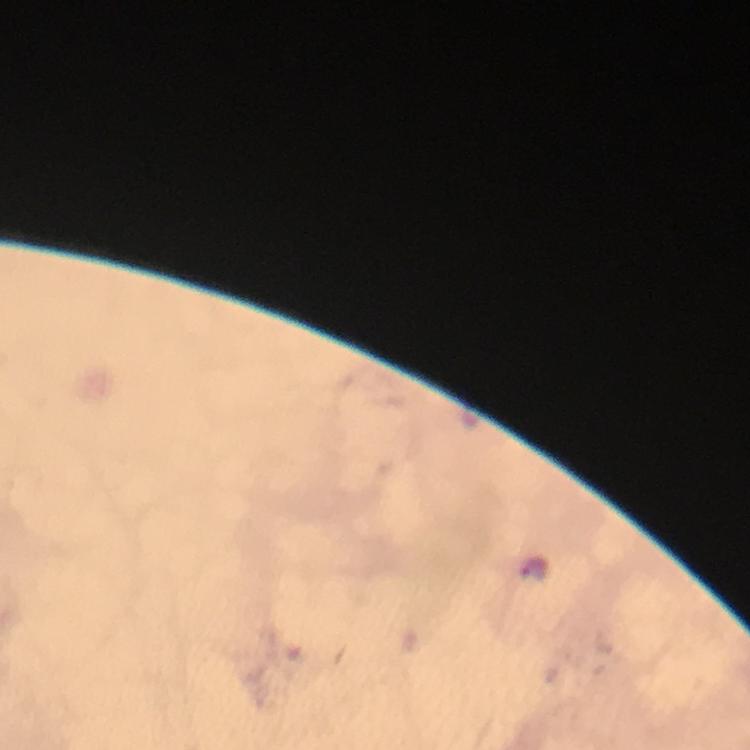
Approximate centers as (x, y) in pixels.
Summary:
  - Malaria parasite locations: (534, 567)
  - Immersion oil: applied
  - Preparation: thick blood smear
  - Cropped from: a single field of view
  - Image size: 750×750 pixels
  - Context: from a diagnostic examination for malaria
  - Magnification: 100x
  - Capture: smartphone mounted on the microscope
  - Stain: Giemsa